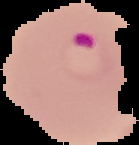
Malaria status: parasitized. Image is 139×145 pixels. Segmented cell region on a black background. From a thin blood film.